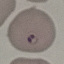
Result: malaria parasites identified. Photographed with a smartphone camera at the microscope eyepiece. Giemsa-stained preparation. Thin blood smear. Automatically extracted cell patch, resized to 64 × 64 pixels.